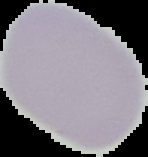
malaria_status: uninfected
image_type: cell region segmented out of the field of view; surrounding area masked to black
image_size: 148×157 pixels
preparation: thin blood smear